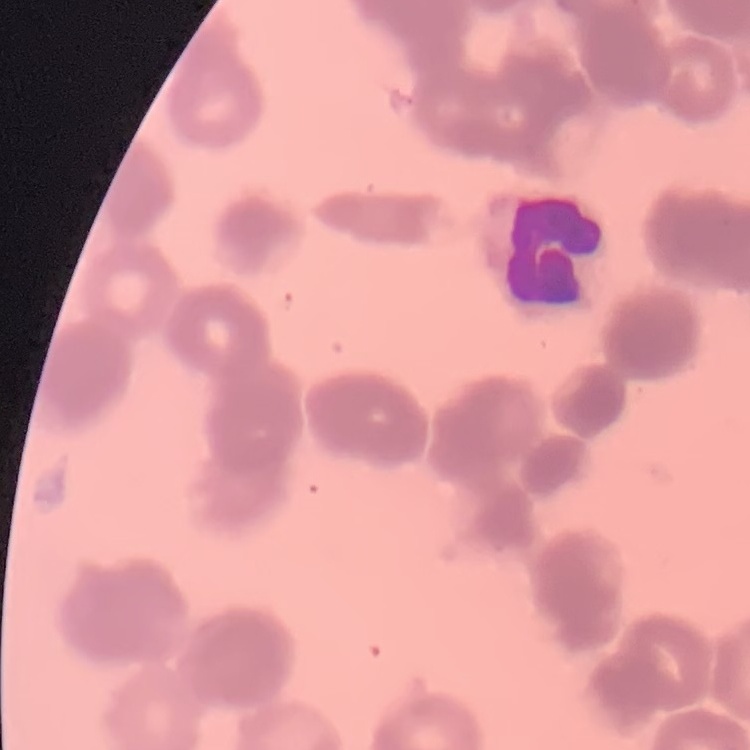
{
  "erythrocyte_morphology": "rouleaux formation",
  "preparation": "thin blood smear",
  "stain": "Field's or Giemsa",
  "image_type": "one tile cut from a larger photomicrograph"
}